Report the malaria status of this cell.
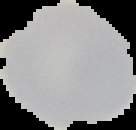
Uninfected.

Summary:
  - Preparation: thin blood smear
  - Image size: 136×130 pixels
  - Image type: segmented cell region with the area outside set to black